Assess for parasitized red blood cells.
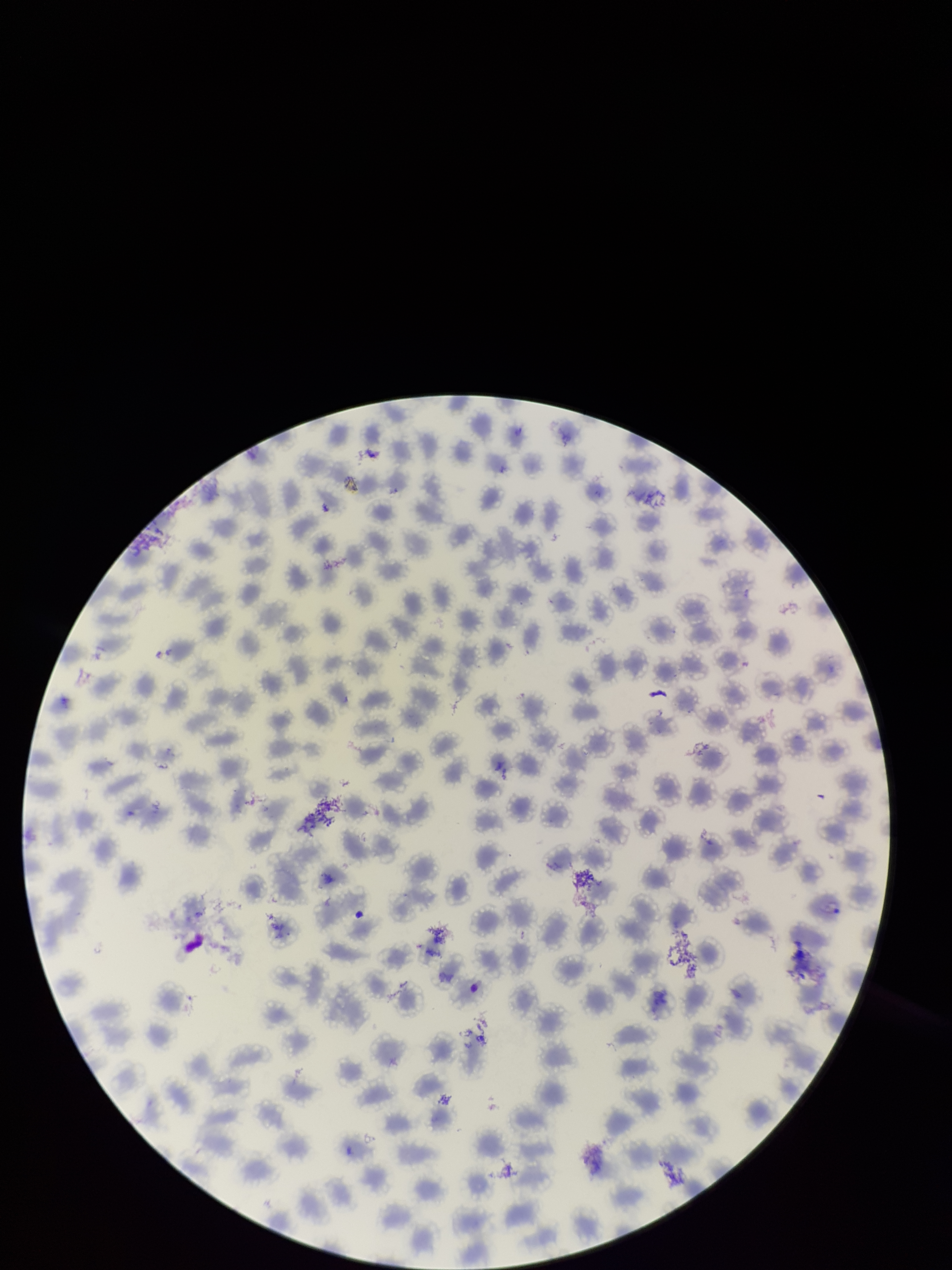

None detected.

Giemsa stain. Preparation: thin smear. Parasitized red blood cell count: 0. One field from this slide. Red blood cell count: 244. Photographed through the microscope eyepiece with a smartphone camera. Image is 952×1270 pixels. Patient malaria status: positive. Species reported for this patient: Plasmodium vivax.